Assess this cell for malaria.
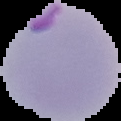
Parasitized.

From a thin blood film. Image is 121×121 pixels. Segmented cell region on a black background.